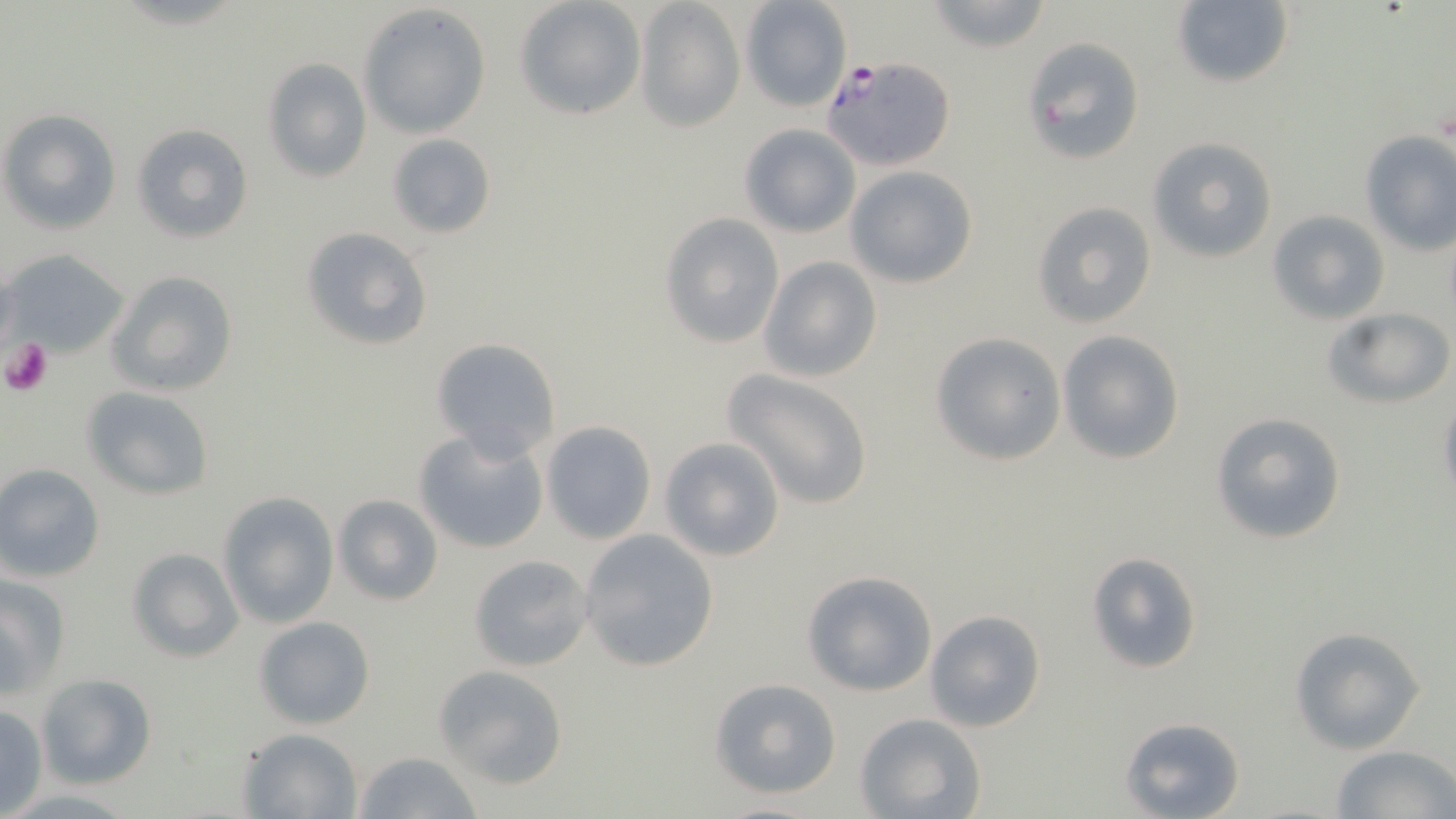 Approximate bounding boxes as (x1, y1, x2, y2) in pixels. Uninfected red blood cell locations (subset): (514, 0, 647, 120), (925, 0, 1056, 53), (634, 1, 746, 133), (739, 1, 853, 111), (1170, 1, 1294, 89), (359, 4, 490, 137), (1020, 37, 1144, 167), (262, 57, 372, 183), (0, 108, 122, 235), (131, 123, 254, 243), (737, 123, 862, 238), (1359, 131, 1456, 255), (387, 133, 496, 239), (1147, 136, 1279, 264), (844, 165, 979, 288), (1030, 201, 1158, 328), (1267, 209, 1391, 325), (658, 214, 784, 349), (300, 227, 433, 352), (5, 251, 128, 357), (759, 257, 881, 383), (105, 270, 239, 397), (1322, 305, 1454, 408), (1056, 330, 1186, 466), (929, 333, 1067, 463), (431, 339, 560, 460), (722, 368, 876, 508), (80, 386, 214, 500), (1436, 395, 1456, 512), (1208, 411, 1347, 544), (541, 420, 657, 543), (413, 428, 550, 556), (659, 436, 785, 562), (0, 464, 106, 582), (217, 491, 339, 629), (332, 493, 445, 607), (578, 528, 720, 673), (125, 546, 244, 662), (1087, 551, 1204, 674), (468, 554, 593, 672), (801, 569, 940, 696), (0, 573, 69, 700), (924, 609, 1046, 733), (254, 616, 376, 731), (1287, 628, 1424, 755), (431, 664, 568, 790), (36, 673, 157, 790), (708, 677, 843, 799), (0, 705, 48, 815), (854, 712, 986, 818), (1120, 716, 1247, 819), (237, 726, 365, 818), (1331, 745, 1455, 819), (355, 750, 484, 819), (708, 799, 833, 819). Platelet locations: (1, 335, 52, 395). Slide-level diagnosis: Plasmodium falciparum. Thin blood smear. May-Grünwald-Giemsa-stained preparation. 1000x magnification. Light microscopy. Single field of view. Image is 1456×819 pixels.